Locate every uninfected red blood cell.
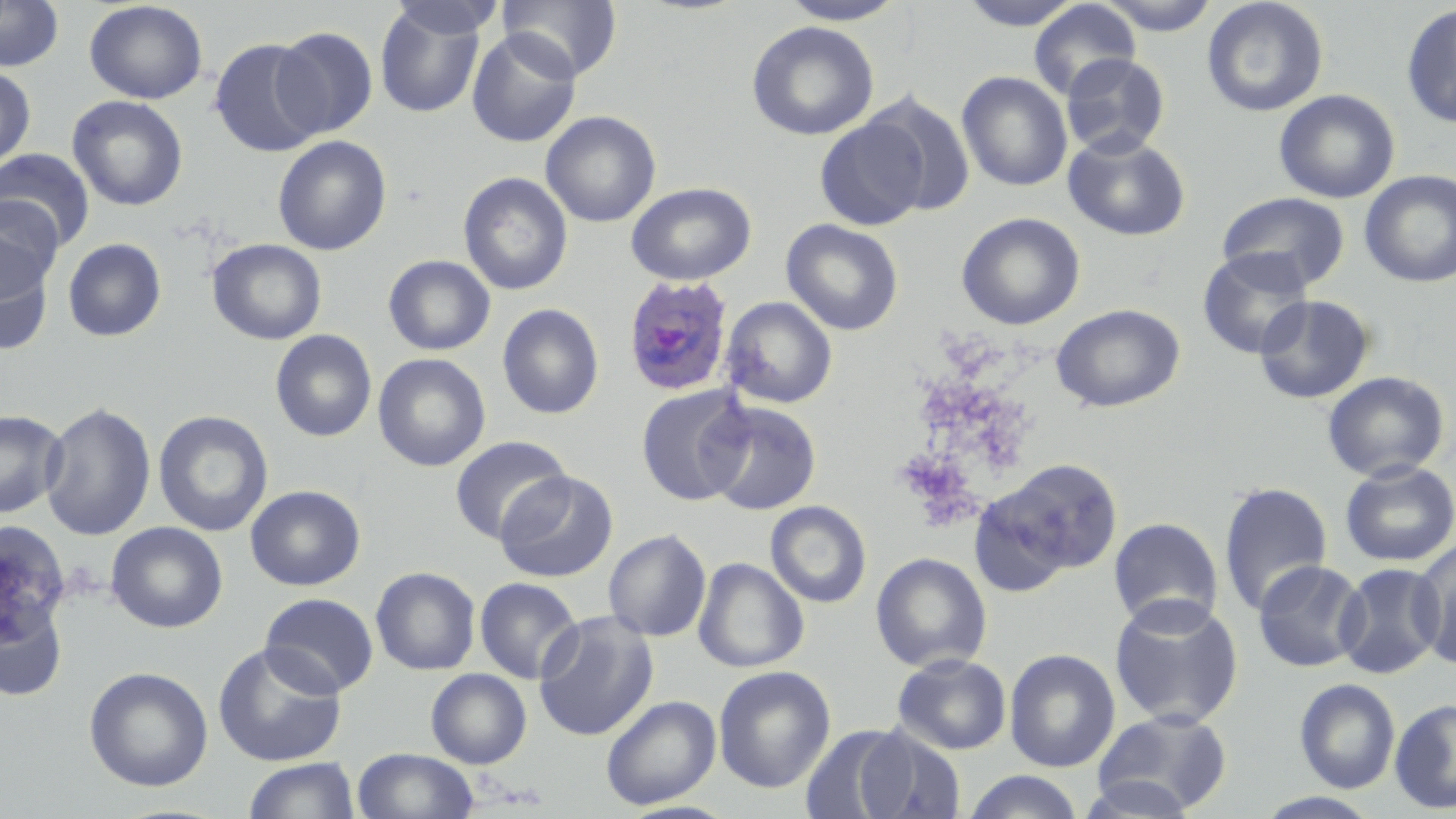

Approximate bounding boxes as (x1, y1, x2, y2) in pixels.
Uninfected red blood cells: (0, 0, 64, 71), (386, 0, 504, 40), (498, 0, 624, 82), (778, 0, 906, 26), (957, 0, 1085, 30), (1095, 0, 1222, 35), (1202, 0, 1329, 117), (84, 1, 208, 104), (1028, 1, 1141, 100), (374, 3, 488, 119), (1401, 4, 1456, 128), (746, 21, 880, 141), (272, 26, 379, 139), (467, 29, 582, 148), (209, 38, 325, 156), (1060, 53, 1170, 158), (0, 65, 36, 170), (956, 71, 1073, 191), (1273, 88, 1400, 204), (862, 91, 977, 217), (67, 94, 189, 211), (540, 110, 661, 227), (814, 117, 929, 231), (1063, 132, 1191, 242), (272, 135, 392, 256), (0, 148, 95, 250), (1359, 170, 1456, 287), (458, 171, 573, 296), (625, 182, 756, 286), (1217, 191, 1351, 291), (0, 196, 64, 296), (956, 212, 1085, 330), (781, 219, 904, 335), (62, 237, 167, 342), (207, 238, 327, 345), (0, 239, 55, 354), (1198, 248, 1314, 360), (383, 254, 496, 356), (1254, 294, 1374, 404), (721, 296, 838, 409), (497, 303, 604, 419), (1051, 303, 1186, 413), (270, 330, 377, 442), (373, 353, 491, 472), (1322, 370, 1450, 482), (636, 384, 752, 506), (702, 400, 822, 515), (39, 402, 156, 542), (0, 409, 67, 518), (153, 409, 274, 537), (450, 436, 573, 545), (988, 458, 1124, 580), (1339, 460, 1456, 567), (494, 470, 619, 582), (1218, 481, 1333, 618), (245, 484, 366, 591), (765, 501, 871, 607), (1108, 517, 1223, 630), (105, 522, 228, 633), (603, 528, 712, 642), (1410, 538, 1456, 668), (870, 551, 992, 672), (693, 558, 809, 673), (1253, 560, 1368, 672), (1334, 562, 1447, 679), (370, 566, 481, 675), (474, 577, 583, 683), (260, 593, 379, 697), (1108, 594, 1244, 729), (0, 597, 68, 702), (533, 610, 658, 742), (212, 643, 347, 767), (1004, 648, 1121, 773), (892, 652, 1012, 755), (713, 665, 836, 794), (83, 666, 213, 792), (425, 669, 532, 768), (1294, 678, 1400, 793), (600, 695, 721, 810), (1390, 697, 1456, 814), (1092, 708, 1232, 815), (853, 726, 965, 819), (352, 748, 479, 819), (242, 757, 361, 819), (962, 771, 1086, 819), (1078, 776, 1199, 818), (1254, 791, 1384, 818).

Plasmodium ovale-infected red blood cell locations: (622, 273, 736, 396). Slide-level diagnosis: Plasmodium ovale. Thin blood film. 1000x magnification. Image is 1456×819 pixels. May-Grünwald-Giemsa stain. Optical microscopy. Single field of view.